Locate every uninfected red blood cell.
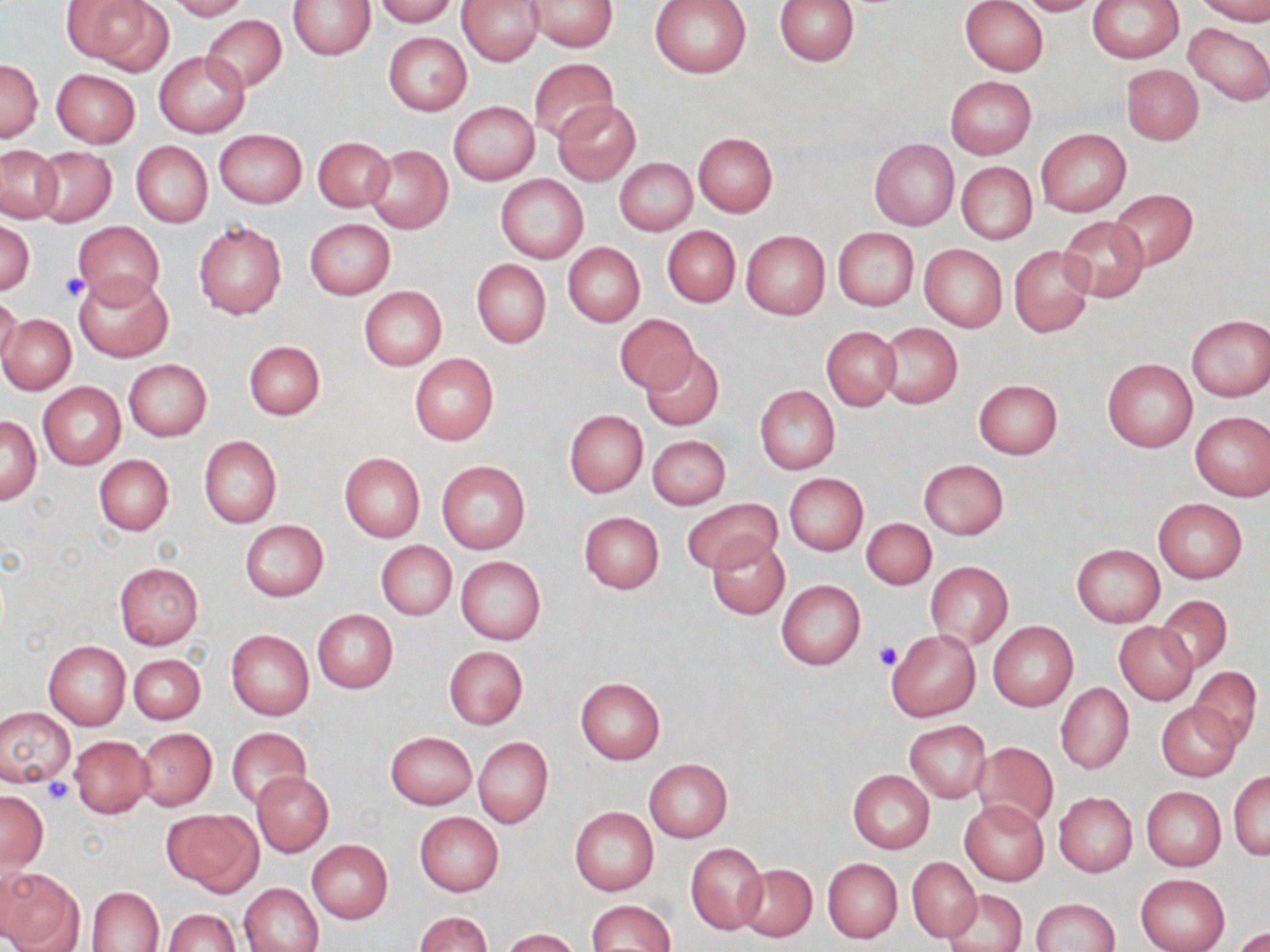
Approximate bounding boxes as (x1,y1)-(x2,y2) corner pairs in pixels.
Uninfected red blood cells: (64,0)-(171,73), (166,0)-(249,20), (374,0)-(457,27), (650,0)-(751,78), (774,0)-(860,66), (961,0)-(1048,76), (1017,0)-(1101,16), (1088,0)-(1183,63), (1194,0)-(1270,24), (290,1)-(376,60), (456,1)-(545,66), (526,1)-(618,51), (200,14)-(286,92), (1183,23)-(1270,105), (382,33)-(471,116), (154,51)-(249,137), (528,58)-(618,142), (0,59)-(42,142), (1121,64)-(1203,145), (52,69)-(140,147), (943,75)-(1036,159), (553,100)-(641,187), (449,101)-(539,185), (1036,127)-(1131,216), (214,129)-(307,208), (693,132)-(777,217), (313,137)-(392,212), (869,139)-(959,231), (131,141)-(212,228), (1,145)-(63,222), (364,145)-(453,234), (34,147)-(115,226), (614,157)-(697,235), (956,162)-(1037,245), (496,175)-(588,263), (1107,189)-(1199,269), (1059,216)-(1149,301), (305,218)-(395,300), (0,219)-(34,295), (73,221)-(163,307), (194,221)-(286,320), (663,226)-(740,308), (833,227)-(918,311), (741,230)-(829,319), (562,243)-(644,327), (919,244)-(1007,333), (1009,244)-(1094,337), (472,260)-(550,349), (73,271)-(174,362), (359,287)-(446,370), (0,294)-(23,374), (1,313)-(75,394), (614,313)-(700,393), (1185,314)-(1270,401), (877,323)-(962,409), (822,326)-(899,410), (243,339)-(326,421), (641,347)-(724,431), (409,354)-(499,446), (1102,358)-(1198,453), (123,359)-(212,442), (973,378)-(1063,459), (39,382)-(125,469), (755,386)-(839,475), (564,410)-(647,497), (1190,412)-(1270,501), (1,415)-(41,504), (199,435)-(281,529), (647,436)-(730,509), (339,452)-(425,542), (94,455)-(173,536), (918,459)-(1009,540), (436,461)-(531,555), (785,473)-(868,556), (681,498)-(781,574), (1153,498)-(1248,584), (579,511)-(665,594), (861,518)-(936,590), (240,520)-(329,601), (706,533)-(789,619), (375,540)-(456,621), (1071,544)-(1164,627), (456,557)-(545,644), (925,561)-(1013,648), (113,562)-(203,650), (776,580)-(865,670), (1157,596)-(1233,672), (312,609)-(397,694), (988,621)-(1078,710), (1115,622)-(1197,705), (226,629)-(314,721), (885,629)-(980,721), (44,640)-(131,730), (444,645)-(528,729), (129,653)-(204,724), (1189,666)-(1262,748), (575,678)-(665,764), (1055,683)-(1133,774), (1156,702)-(1241,781), (0,707)-(74,786), (905,721)-(990,803), (136,727)-(216,810), (227,727)-(312,810), (385,731)-(476,810), (70,736)-(153,817), (473,737)-(553,829), (971,741)-(1058,832), (644,759)-(733,841), (847,770)-(934,854), (252,771)-(333,856), (1229,771)-(1270,860), (1141,787)-(1225,870), (0,791)-(48,872), (1053,792)-(1138,877), (958,799)-(1048,887), (569,807)-(658,896), (163,808)-(263,895), (414,812)-(504,896), (307,840)-(393,924), (686,842)-(767,936), (907,857)-(981,941), (823,858)-(902,943), (737,863)-(817,942), (0,865)-(84,952), (1135,873)-(1230,952), (239,882)-(323,952), (86,886)-(164,951), (945,890)-(1027,952), (1030,898)-(1119,952), (585,900)-(675,952), (162,908)-(239,952), (413,911)-(492,952), (1231,927)-(1270,952), (500,928)-(581,952).

slide_level_diagnosis: no evidence of blood parasites
stain: May-Grünwald-Giemsa
field_of_view: one of a larger specimen
image_size: 1270×952 pixels
modality: optical microscopy
preparation: thin blood smear
magnification: 1000x
platelet_locations: 'approximate bounding boxes as (x1,y1)-(x2,y2) corner pairs in pixels: (58,272)-(91,303), (872,639)-(902,671), (43,778)-(75,806)'